State which parasite is depicted.
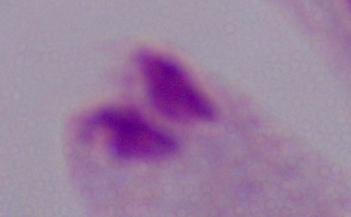
A trichomonad.

Captured at 1000x magnification. Photomicrograph.